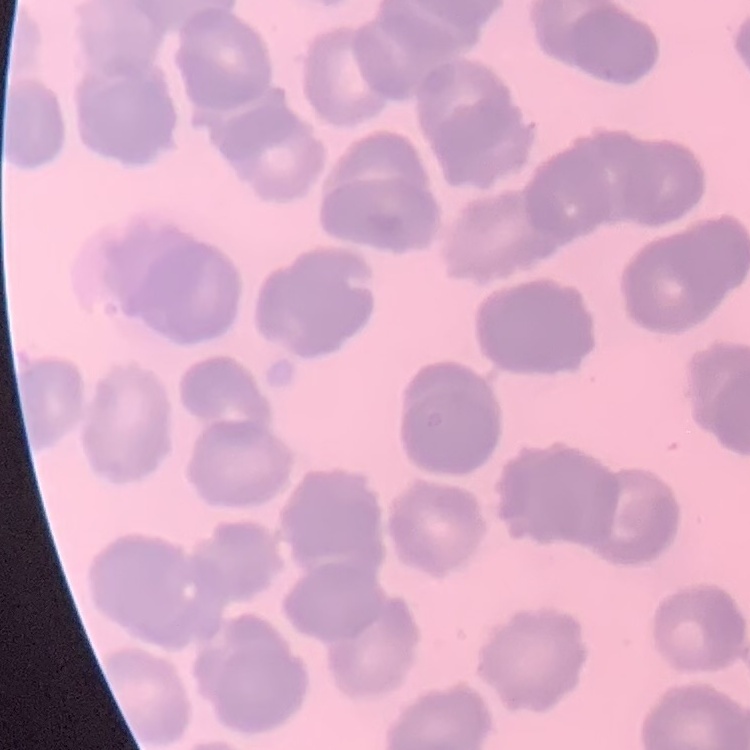

erythrocyte morphology = rouleaux formation
preparation = thin blood film
image type = square crop of a larger photomicrograph
stain = Field's or Giemsa